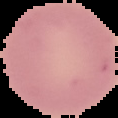

From a thin blood film. Result: negative for malaria parasites. The area outside the segmented cell region is set to black. Image is 118×118 pixels.